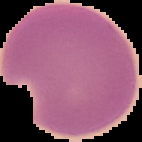
Summary:
  - Result: no Plasmodium parasites seen
  - Image size: 142×142 pixels
  - Preparation: thin blood smear
  - Image type: cell region segmented out of the field of view; surrounding area masked to black